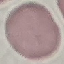
Result: no malaria parasites detected. Giemsa-stained preparation. Thin blood smear. Photographed with a smartphone camera at the microscope eyepiece. Automatically extracted cell patch, resized to 64 × 64 pixels.